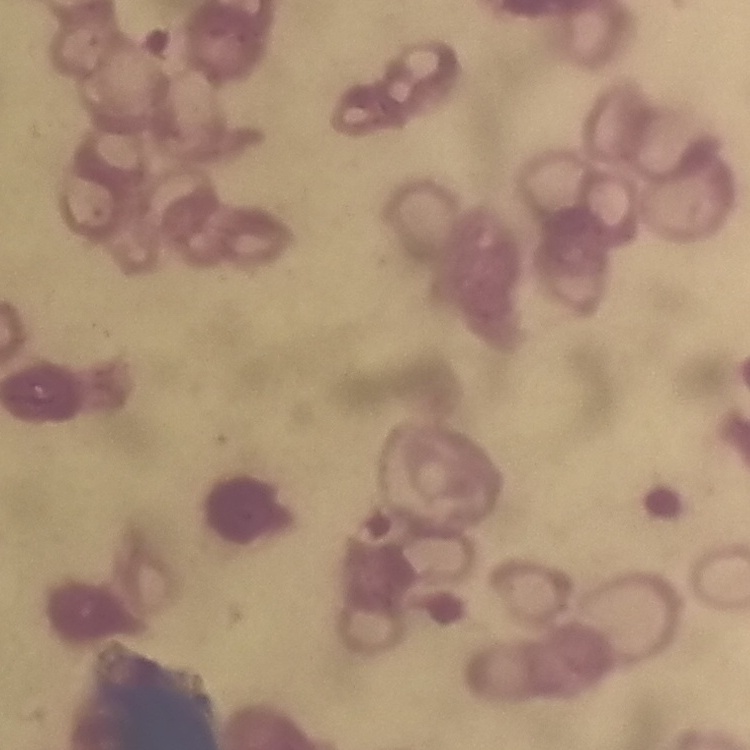
red blood cell morphology = rouleaux formation
stain = Field's or Giemsa
image type = square crop of a larger photomicrograph
preparation = thin blood film